Describe the morphology of the red blood cells.
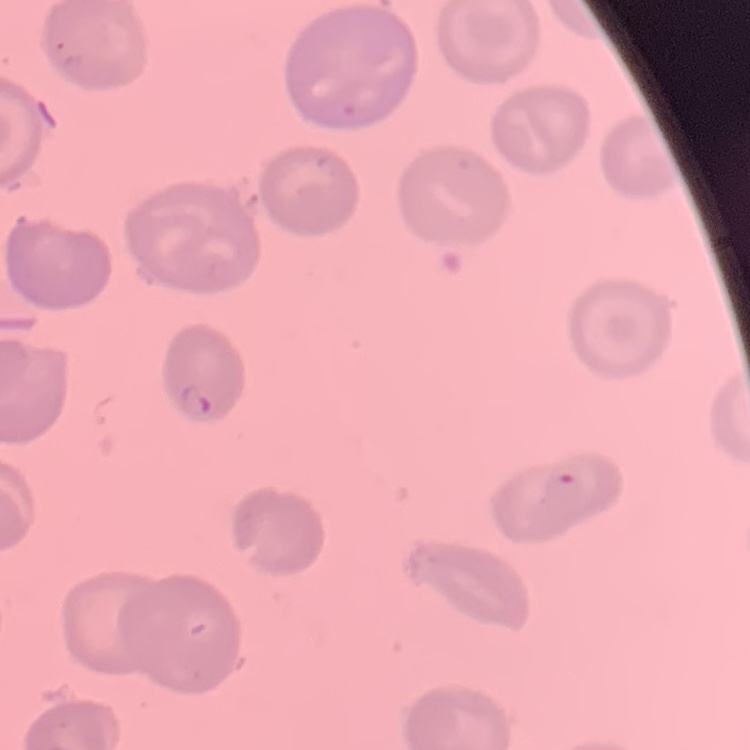

No rouleaux formation.

One tile cut from a larger photomicrograph. Field's or Giemsa stain. Thin blood smear.